Describe the morphology of the erythrocytes.
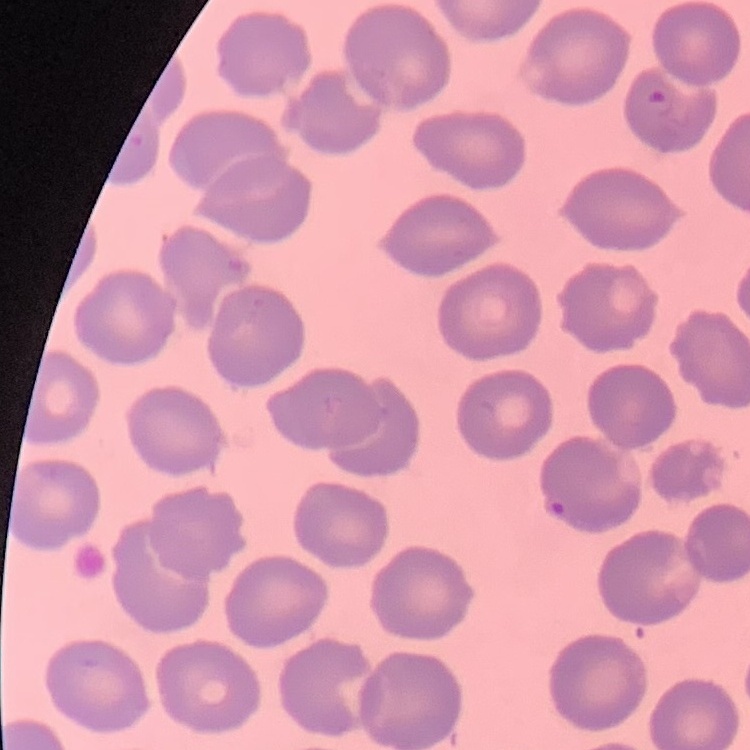
They show no rouleaux formation.

{
  "image_type": "square crop of a larger photomicrograph",
  "stain": "Field's or Giemsa",
  "preparation": "thin blood smear"
}